Assess this cell for malaria.
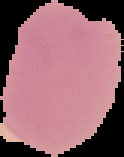

It is uninfected.

Summary:
  - Image type: cell region segmented out of the field of view; surrounding area masked to black
  - Image size: 124×157 pixels
  - Preparation: thin blood smear